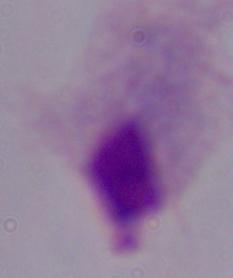

magnification: 1000x
identification: trichomonad
modality: photomicrograph